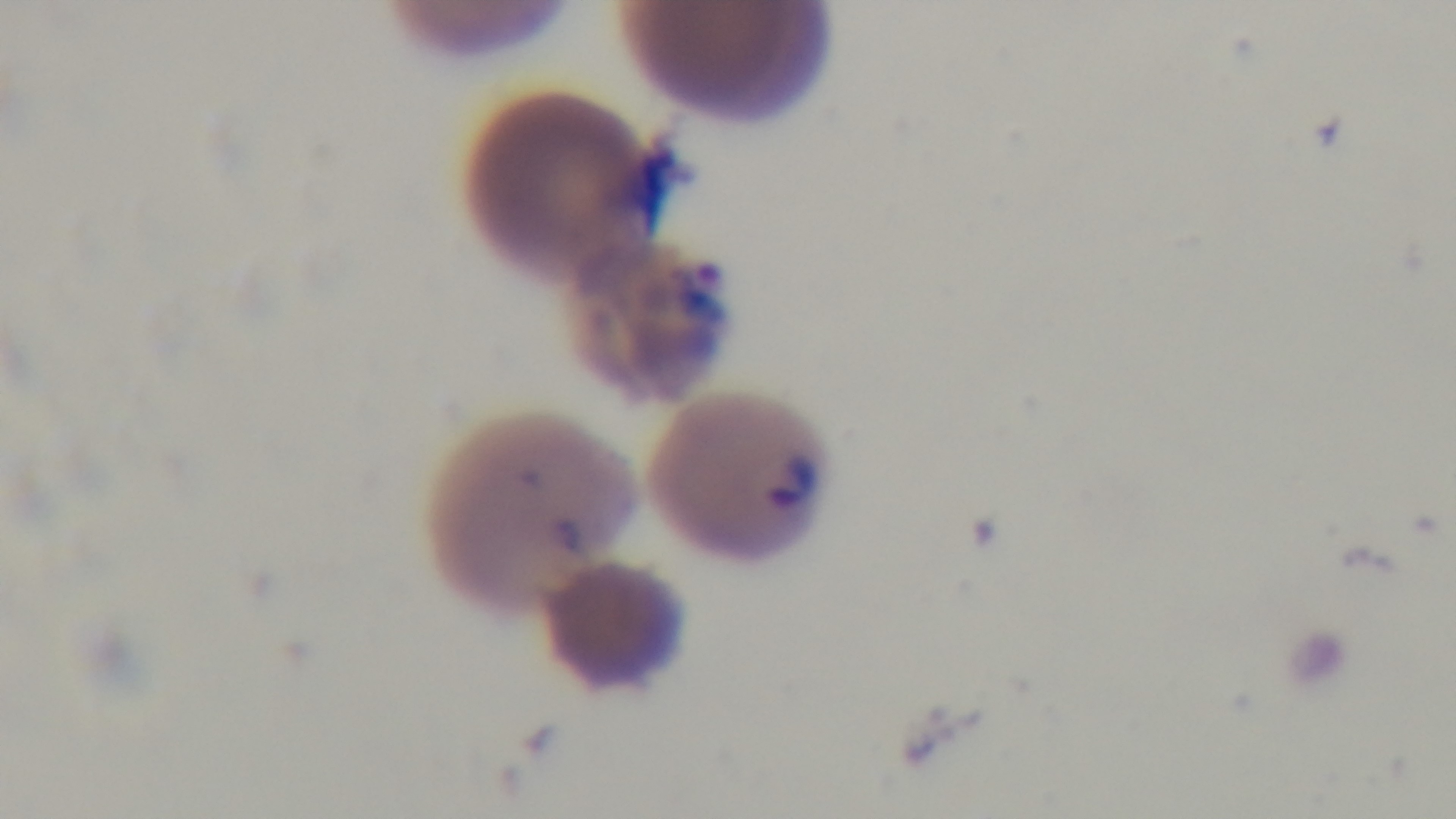 100x oil-immersion objective. One field from the slide. Malaria status: positive. Giemsa stain. Mounted 4K digital camera. Photomicrograph. Preparation: thin blood film.